Locate every malaria parasite.
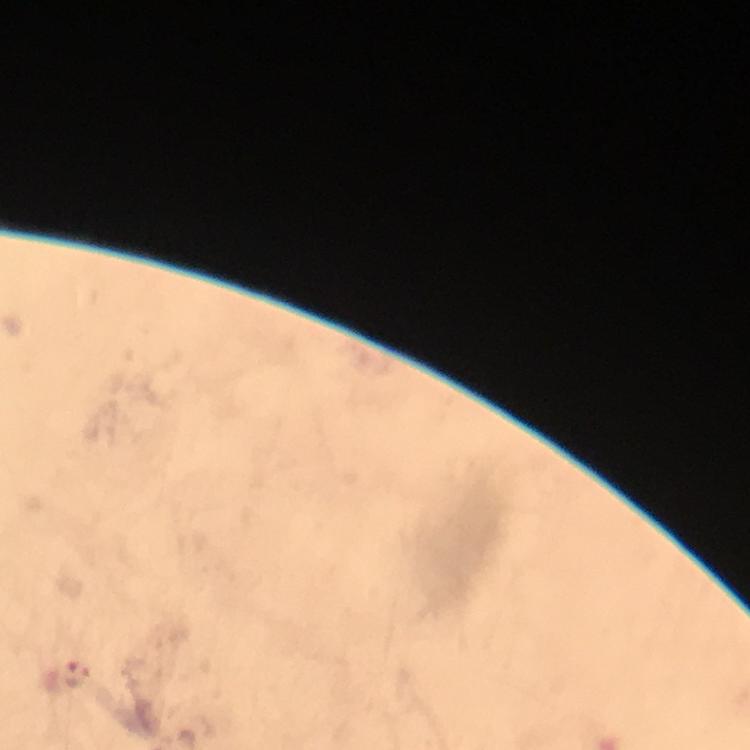

Approximate centers as (x, y) in pixels.
Malaria parasites: (77, 675).

Summary:
  - Context: from a malaria diagnostic workup
  - Cropped from: one field of view
  - Preparation: thick blood film
  - Stain: Giemsa
  - Capture: smartphone photograph through a microscope
  - Image size: 750×750 pixels
  - Magnification: 100x
  - Immersion oil: applied